Give the position of every Plasmodium parasite visible.
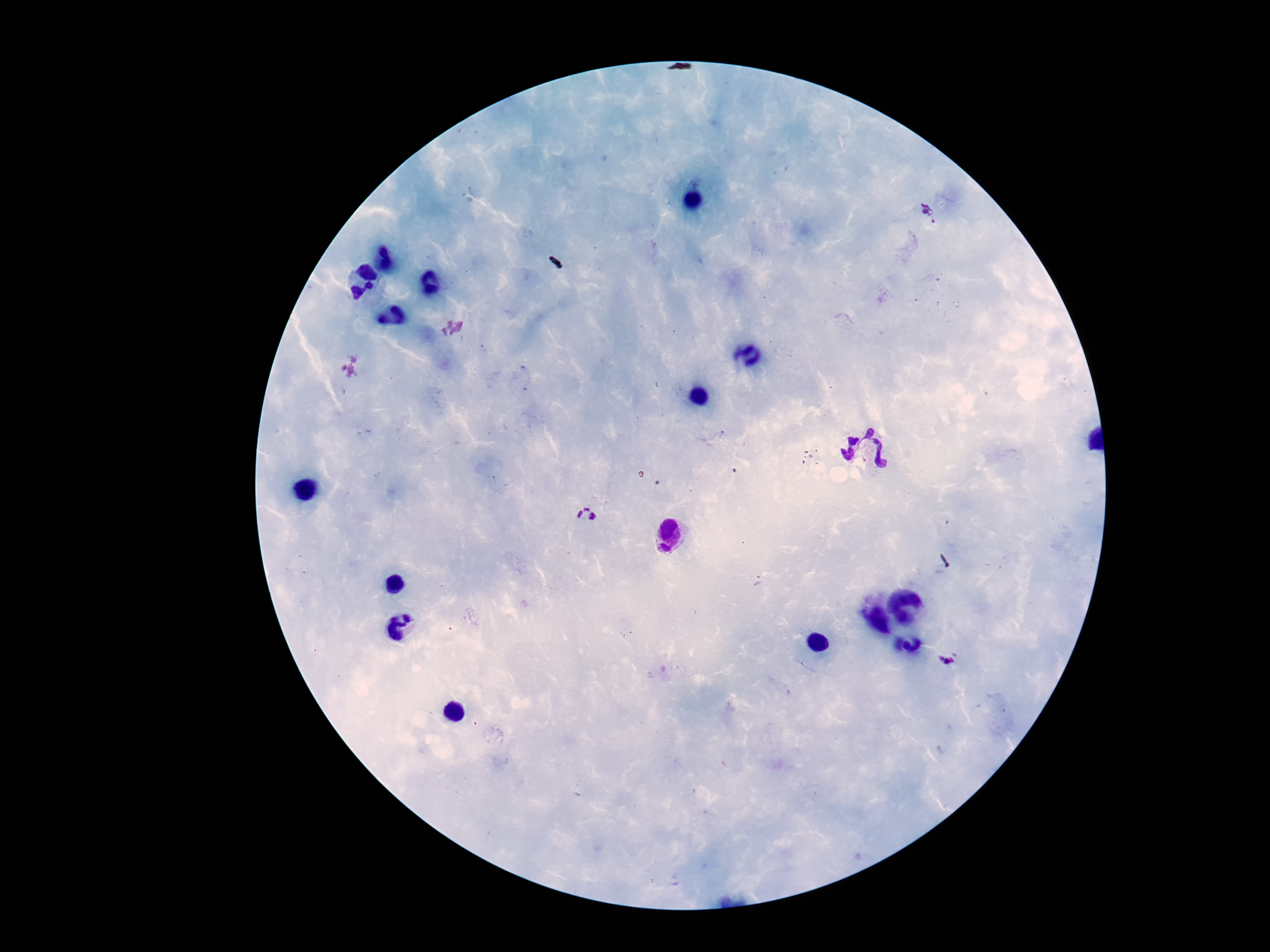
Approximate centers as (x, y) in pixels.
Plasmodium parasites: (927, 213), (586, 515), (947, 659).

One field from this slide. 100x magnification. Thick blood smear. Giemsa-stained preparation. Patient malaria status: infected. Image is 1270×952 pixels. Photographed through the microscope eyepiece with a smartphone camera.